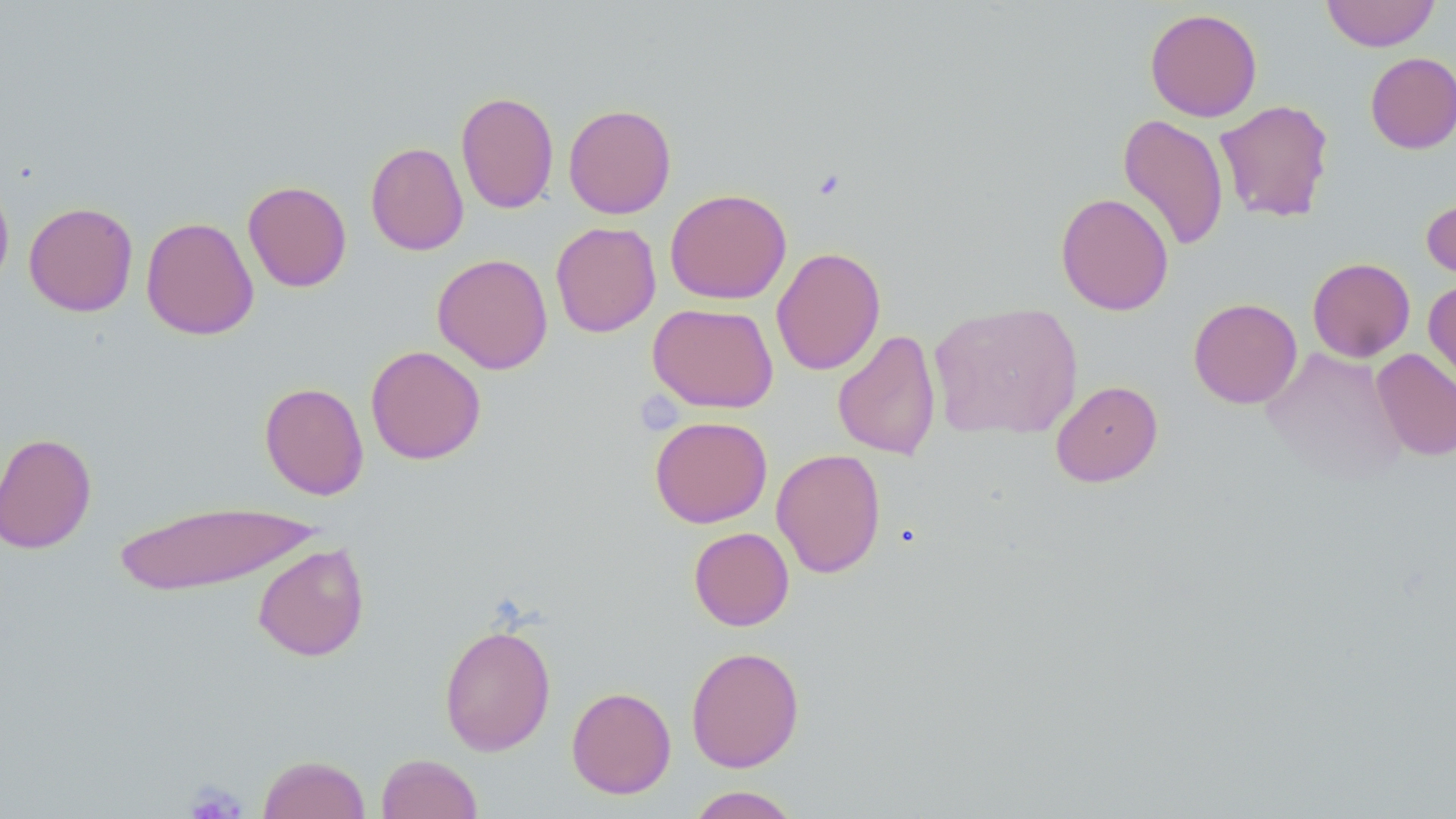
Approximate bounding boxes as (x1,y1)-(x2,y2) corner pairs in pixels. Uninfected red blood cell locations: (1321,0)-(1439,51), (1145,7)-(1263,122), (1366,52)-(1456,153), (456,91)-(559,214), (1214,99)-(1334,223), (563,103)-(676,219), (1117,114)-(1229,252), (365,141)-(469,256), (0,175)-(14,292), (242,180)-(352,292), (665,188)-(791,304), (1056,192)-(1174,316), (1421,192)-(1456,286), (23,201)-(138,317), (140,216)-(259,341), (550,221)-(661,338), (771,247)-(886,375), (432,253)-(553,375), (1307,257)-(1415,362), (1423,278)-(1456,394), (1188,297)-(1302,408), (928,301)-(1083,441), (647,302)-(778,413), (832,329)-(941,461), (366,345)-(486,465), (1261,347)-(1409,484), (1372,348)-(1456,461), (1050,380)-(1163,488), (259,382)-(369,500), (649,415)-(773,528), (0,431)-(97,554), (771,448)-(886,578), (112,499)-(321,596), (688,527)-(794,631), (252,542)-(370,661), (439,622)-(557,756), (685,646)-(804,772), (566,686)-(677,799), (376,753)-(482,818), (257,754)-(371,818), (686,785)-(803,818). Platelet locations: (184,782)-(249,818). Slide-level diagnosis: no evidence of blood parasites. May-Grünwald-Giemsa stain. Single field of view. Image is 1456×819 pixels. Captured at 1000x magnification. Thin blood smear. Light microscopy.